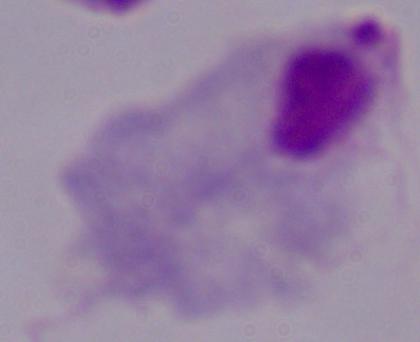

A trichomonad is seen. 1000x magnification. Photomicrograph.